Identify the blood parasite species.
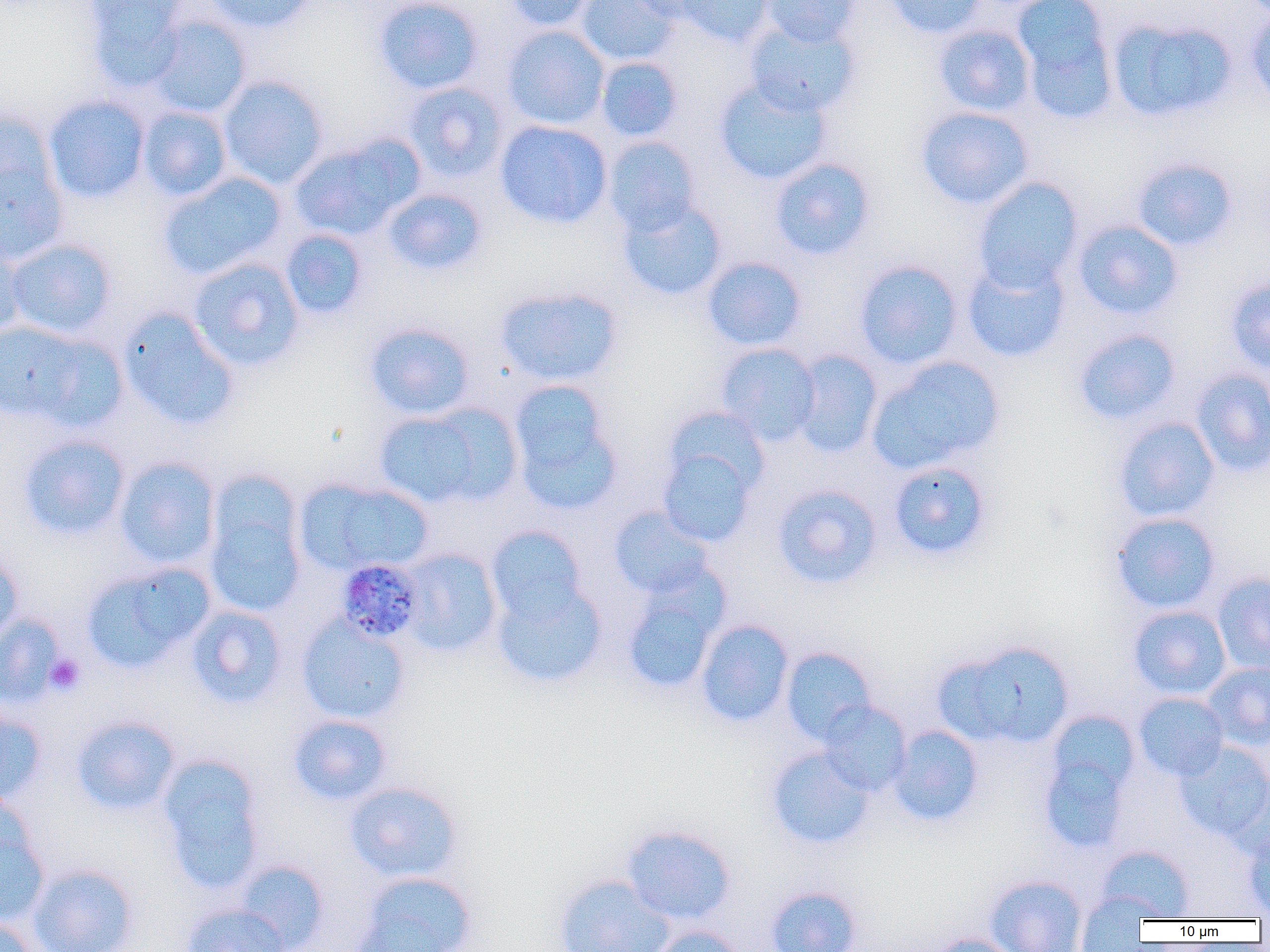
Plasmodium malariae.

Approximate bounding boxes as named x1/y1/x2/y2 corners in pixels. Platelet locations: (x1=43, y1=653, x2=86, y2=696). Uninfected red blood cell locations: (x1=82, y1=0, x2=192, y2=88), (x1=202, y1=0, x2=317, y2=33), (x1=373, y1=0, x2=485, y2=94), (x1=501, y1=0, x2=598, y2=32), (x1=575, y1=0, x2=681, y2=66), (x1=623, y1=0, x2=719, y2=22), (x1=672, y1=0, x2=773, y2=47), (x1=758, y1=0, x2=862, y2=47), (x1=881, y1=0, x2=987, y2=39), (x1=1016, y1=3, x2=1118, y2=123), (x1=1246, y1=6, x2=1270, y2=105), (x1=146, y1=15, x2=252, y2=118), (x1=1108, y1=17, x2=1238, y2=122), (x1=744, y1=18, x2=862, y2=117), (x1=933, y1=24, x2=1036, y2=116), (x1=502, y1=25, x2=610, y2=130), (x1=595, y1=56, x2=683, y2=141), (x1=217, y1=75, x2=329, y2=189), (x1=713, y1=77, x2=833, y2=185), (x1=402, y1=82, x2=509, y2=183), (x1=44, y1=95, x2=151, y2=204), (x1=138, y1=106, x2=232, y2=201), (x1=915, y1=106, x2=1034, y2=209), (x1=0, y1=108, x2=60, y2=207), (x1=495, y1=120, x2=612, y2=228), (x1=289, y1=135, x2=420, y2=240), (x1=602, y1=136, x2=702, y2=234), (x1=770, y1=157, x2=875, y2=260), (x1=1131, y1=157, x2=1238, y2=251), (x1=0, y1=158, x2=68, y2=265), (x1=159, y1=172, x2=287, y2=281), (x1=972, y1=177, x2=1084, y2=292), (x1=382, y1=188, x2=488, y2=275), (x1=618, y1=199, x2=728, y2=301), (x1=1072, y1=219, x2=1184, y2=321), (x1=280, y1=228, x2=369, y2=320), (x1=0, y1=237, x2=28, y2=338), (x1=4, y1=238, x2=119, y2=339), (x1=702, y1=256, x2=807, y2=351), (x1=188, y1=257, x2=305, y2=372), (x1=961, y1=257, x2=1070, y2=363), (x1=853, y1=259, x2=963, y2=369), (x1=1225, y1=276, x2=1270, y2=375), (x1=494, y1=286, x2=623, y2=386), (x1=118, y1=309, x2=240, y2=430), (x1=364, y1=321, x2=476, y2=420), (x1=0, y1=322, x2=112, y2=426), (x1=1072, y1=328, x2=1181, y2=425), (x1=716, y1=343, x2=820, y2=446), (x1=790, y1=349, x2=883, y2=458), (x1=868, y1=356, x2=1004, y2=473), (x1=1190, y1=368, x2=1270, y2=477), (x1=507, y1=379, x2=623, y2=514), (x1=373, y1=406, x2=506, y2=508), (x1=663, y1=406, x2=770, y2=497), (x1=1113, y1=416, x2=1220, y2=522), (x1=17, y1=433, x2=131, y2=541), (x1=657, y1=445, x2=759, y2=546), (x1=115, y1=456, x2=220, y2=570), (x1=887, y1=460, x2=993, y2=561), (x1=203, y1=471, x2=307, y2=620), (x1=295, y1=477, x2=432, y2=576), (x1=771, y1=484, x2=883, y2=589), (x1=608, y1=505, x2=714, y2=598), (x1=1110, y1=512, x2=1221, y2=614), (x1=485, y1=525, x2=588, y2=626), (x1=399, y1=548, x2=502, y2=657), (x1=0, y1=549, x2=23, y2=647), (x1=81, y1=562, x2=214, y2=674), (x1=1211, y1=571, x2=1270, y2=674), (x1=491, y1=579, x2=607, y2=689), (x1=620, y1=580, x2=726, y2=695), (x1=186, y1=605, x2=288, y2=709), (x1=1128, y1=605, x2=1231, y2=700), (x1=0, y1=612, x2=65, y2=706), (x1=296, y1=615, x2=412, y2=724), (x1=695, y1=619, x2=794, y2=727), (x1=937, y1=641, x2=1075, y2=749), (x1=781, y1=647, x2=877, y2=746), (x1=1202, y1=662, x2=1270, y2=750), (x1=1133, y1=692, x2=1229, y2=781), (x1=818, y1=701, x2=912, y2=795), (x1=0, y1=705, x2=47, y2=805), (x1=289, y1=714, x2=392, y2=806), (x1=1038, y1=714, x2=1140, y2=851), (x1=71, y1=716, x2=181, y2=815), (x1=889, y1=725, x2=984, y2=827), (x1=1174, y1=741, x2=1270, y2=843), (x1=765, y1=747, x2=875, y2=849), (x1=157, y1=755, x2=267, y2=893), (x1=1224, y1=775, x2=1270, y2=861), (x1=344, y1=781, x2=463, y2=882), (x1=0, y1=821, x2=50, y2=926), (x1=621, y1=824, x2=737, y2=925), (x1=1243, y1=830, x2=1270, y2=917), (x1=1097, y1=845, x2=1195, y2=920), (x1=235, y1=860, x2=329, y2=952), (x1=29, y1=863, x2=139, y2=952), (x1=356, y1=871, x2=477, y2=952), (x1=553, y1=873, x2=674, y2=952), (x1=985, y1=875, x2=1088, y2=952), (x1=765, y1=885, x2=863, y2=952), (x1=1075, y1=891, x2=1158, y2=951), (x1=180, y1=903, x2=291, y2=952), (x1=0, y1=915, x2=40, y2=952), (x1=649, y1=925, x2=746, y2=952), (x1=927, y1=933, x2=1021, y2=952). Plasmodium malariae-infected red blood cell locations: (x1=332, y1=560, x2=421, y2=645). 1000x magnification. Thin blood smear. Single field of view. Image is 1270×952 pixels. Optical microscopy.